Outline each uninfected red blood cell.
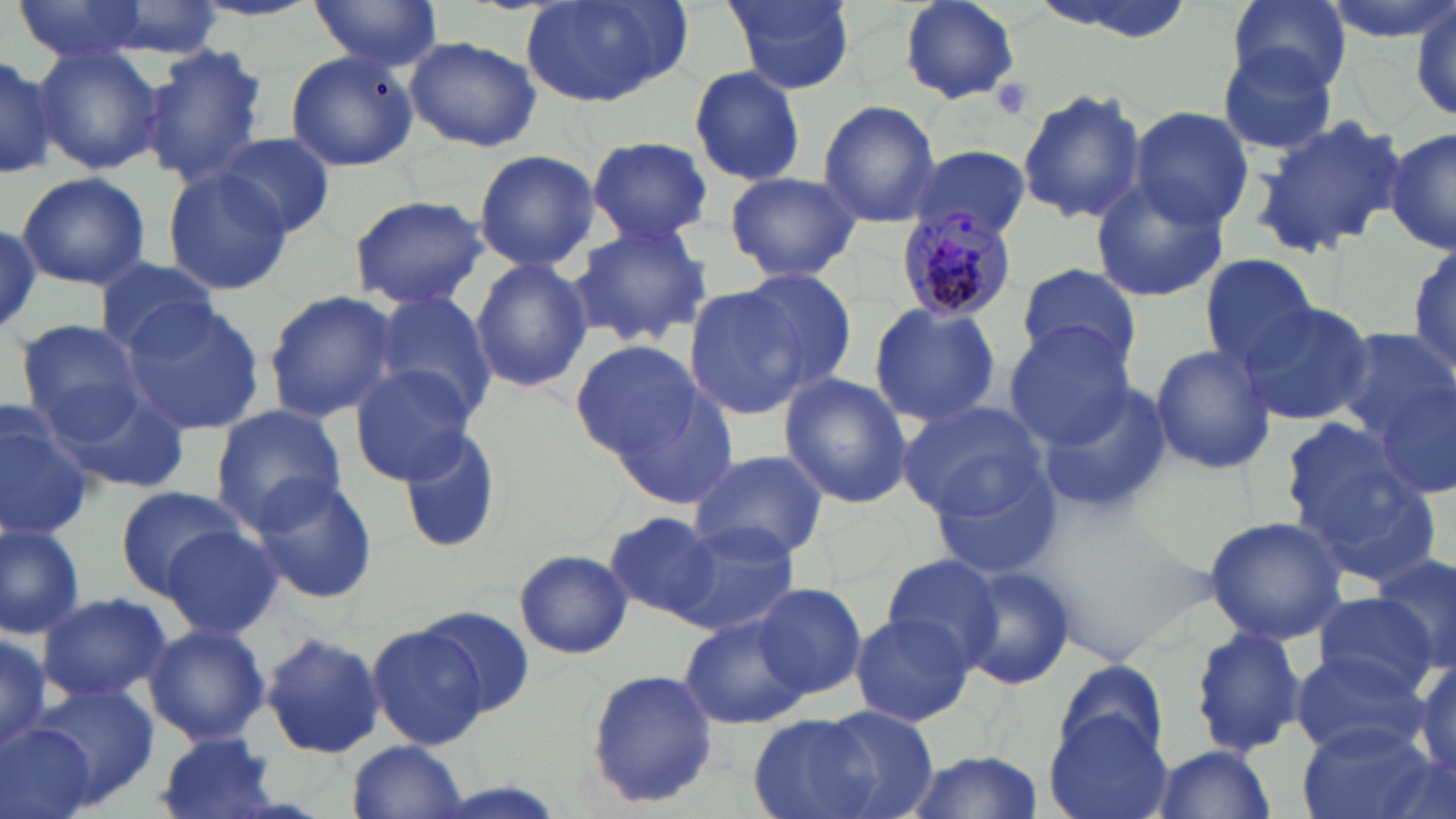

Approximate bounding boxes as [x1, y1, x2, y2] in pixels.
Uninfected red blood cells: [10, 0, 159, 62], [306, 0, 444, 70], [522, 0, 689, 109], [721, 0, 857, 95], [898, 0, 1020, 105], [1221, 0, 1352, 96], [1316, 0, 1456, 43], [1409, 0, 1456, 121], [88, 1, 228, 58], [405, 35, 541, 152], [1216, 43, 1344, 158], [30, 45, 163, 175], [143, 45, 267, 183], [285, 47, 416, 172], [0, 49, 66, 179], [688, 65, 805, 187], [1018, 87, 1145, 224], [817, 101, 942, 229], [1130, 107, 1253, 230], [1252, 116, 1409, 256], [1386, 127, 1455, 256], [212, 134, 334, 237], [583, 137, 717, 248], [906, 145, 1031, 244], [472, 149, 599, 273], [160, 167, 294, 297], [15, 170, 151, 289], [723, 171, 862, 282], [1090, 176, 1230, 303], [346, 194, 490, 315], [0, 215, 44, 340], [570, 220, 711, 348], [1408, 241, 1456, 381], [1199, 255, 1320, 372], [470, 257, 592, 396], [91, 258, 222, 354], [1016, 263, 1141, 374], [728, 267, 859, 396], [683, 286, 815, 421], [263, 290, 399, 422], [369, 291, 500, 423], [115, 300, 265, 434], [867, 300, 1002, 427], [1238, 301, 1375, 427], [16, 319, 148, 436], [1004, 324, 1137, 448], [1329, 329, 1456, 443], [572, 341, 702, 461], [1148, 344, 1277, 474], [349, 365, 476, 485], [778, 374, 914, 507], [607, 377, 742, 510], [1370, 380, 1456, 498], [1034, 382, 1174, 520], [52, 385, 193, 495], [896, 400, 1049, 519], [210, 404, 346, 531], [0, 410, 95, 541], [397, 426, 504, 554], [1281, 433, 1437, 577], [688, 449, 829, 565], [929, 462, 1062, 581], [250, 472, 377, 604], [116, 484, 246, 594], [607, 512, 724, 620], [1203, 515, 1351, 645], [0, 521, 87, 639], [670, 522, 801, 635], [159, 526, 283, 640], [513, 548, 632, 659], [1369, 552, 1456, 669], [879, 553, 1002, 668], [951, 561, 1075, 691], [751, 581, 868, 702], [37, 591, 170, 704], [1316, 595, 1439, 700], [419, 606, 536, 716], [848, 612, 974, 728], [680, 615, 811, 730], [143, 623, 270, 746], [366, 624, 489, 751], [1190, 625, 1307, 758], [0, 627, 51, 754], [259, 631, 385, 758], [0, 632, 51, 749], [1288, 651, 1426, 757], [1410, 659, 1456, 782], [1052, 660, 1170, 768], [586, 669, 721, 808], [31, 684, 157, 805], [799, 707, 936, 819], [1045, 713, 1171, 819], [748, 714, 882, 819], [0, 723, 97, 819], [1298, 724, 1436, 819], [154, 733, 283, 819], [347, 740, 467, 819], [1150, 744, 1276, 818], [897, 750, 1046, 819].

Platelet locations: [986, 76, 1036, 121]. Plasmodium malariae-infected red blood cell locations: [898, 214, 1019, 325]. Slide-level diagnosis: Plasmodium malariae. Light microscopy. 1000x magnification. Image is 1456×819 pixels. Single field of view. May-Grünwald-Giemsa-stained preparation. Thin blood smear.